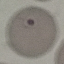

Summary:
  - Malaria status: uninfected
  - Image type: automatically extracted cell patch, resized to 64 × 64 pixels
  - Stain: Giemsa
  - Preparation: thin smear
  - Capture: smartphone camera at the microscope eyepiece